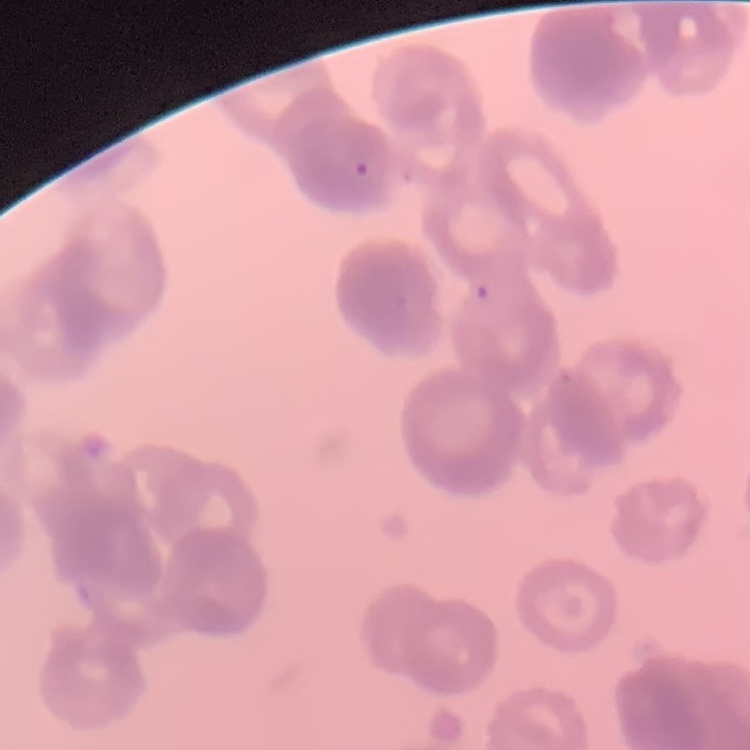
Summary:
  - Erythrocyte morphology: rouleaux formation
  - Preparation: thin blood film
  - Stain: Field's or Giemsa
  - Image type: square crop of a larger photomicrograph